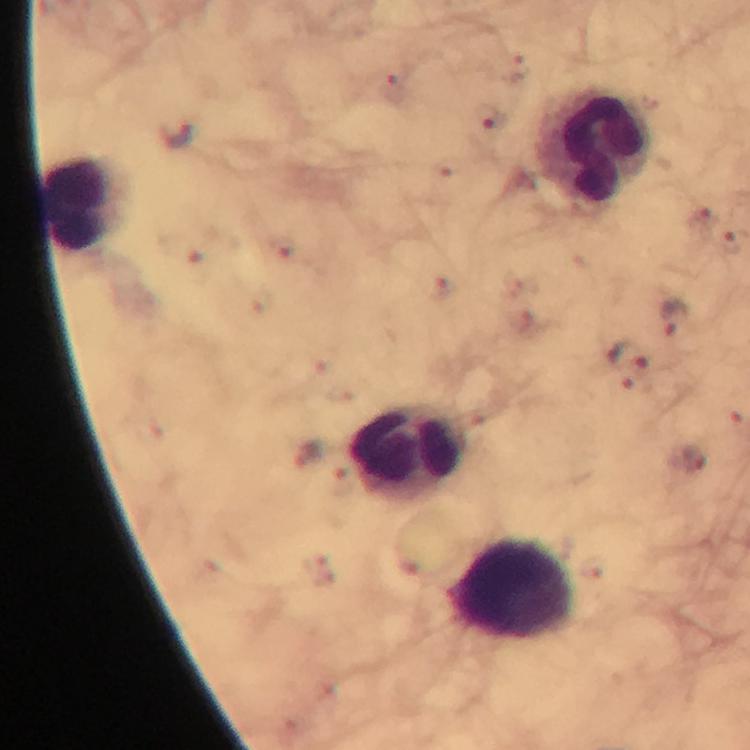

Approximate object centers, in pixels from the top-left corner.
Summary:
  - Plasmodium parasite locations: (x=392, y=88), (x=491, y=117), (x=177, y=134), (x=702, y=223), (x=730, y=245), (x=675, y=315), (x=628, y=355), (x=307, y=454), (x=690, y=458)
  - Leukocyte locations: (x=593, y=146), (x=83, y=205), (x=407, y=453), (x=513, y=588)
  - Image size: 750×750 pixels
  - Context: from a malaria diagnostic workup
  - Immersion oil: used
  - Preparation: thick blood smear
  - Capture: smartphone photograph through a microscope
  - Cropped from: one field of view
  - Stain: Giemsa
  - Magnification: 100x